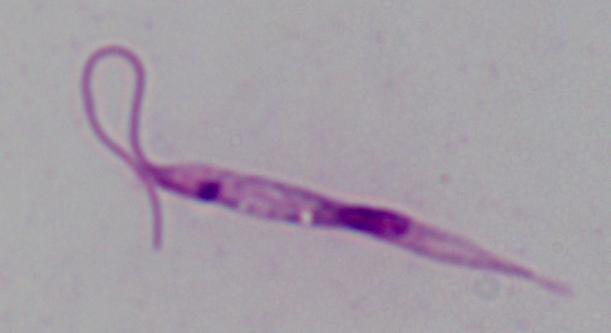
Summary:
  - Modality: micrograph
  - Identification: Leishmania
  - Magnification: 1000x